Report the malaria status of this cell.
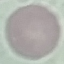

It is uninfected.

stain = Giemsa
image type = cell patch, automatically extracted from a larger field of view and resized to 64 × 64 pixels
preparation = thin blood smear
capture = smartphone through the microscope eyepiece